Comment on the morphology of the red blood cells.
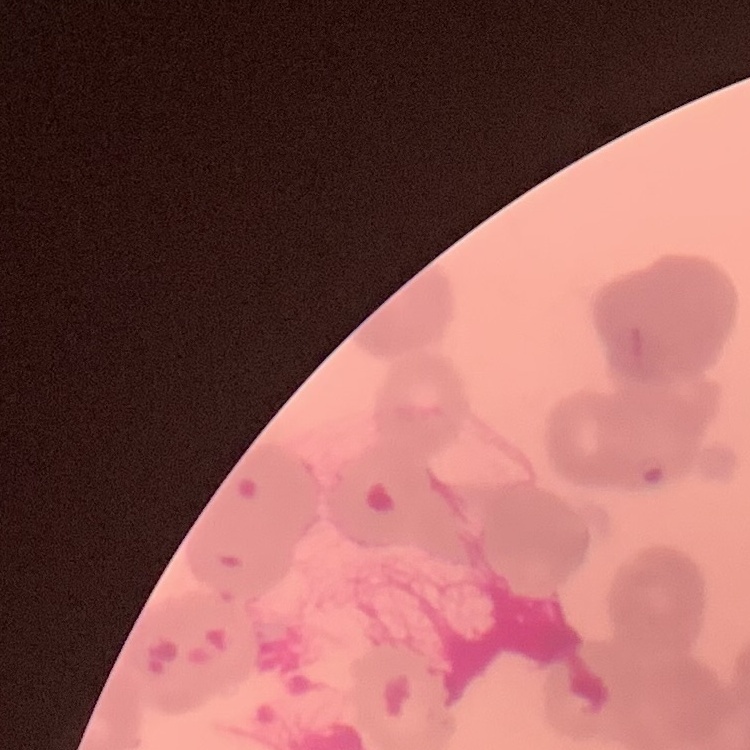
Rouleaux formation.

Square crop of a larger photomicrograph. Field's or Giemsa stain. Thin blood smear.